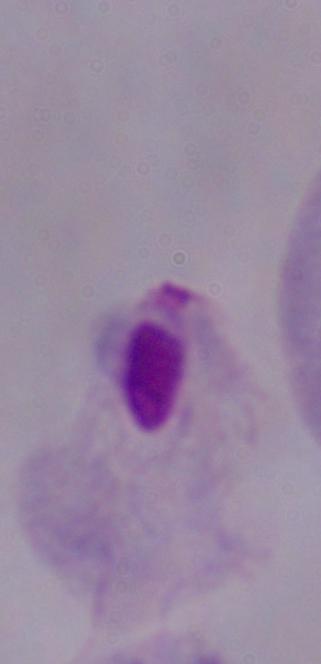
Summary:
  - Modality: photomicrograph
  - Magnification: 1000x
  - Identification: trichomonad